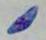

Toxoplasma gondii is seen. Captured at 1000x magnification. Micrograph.